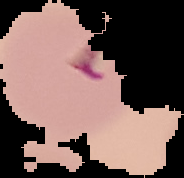
Summary:
  - Result: malaria parasites detected
  - Preparation: thin blood film
  - Image size: 184×178 pixels
  - Image type: cell region segmented out of the field of view; surrounding area masked to black